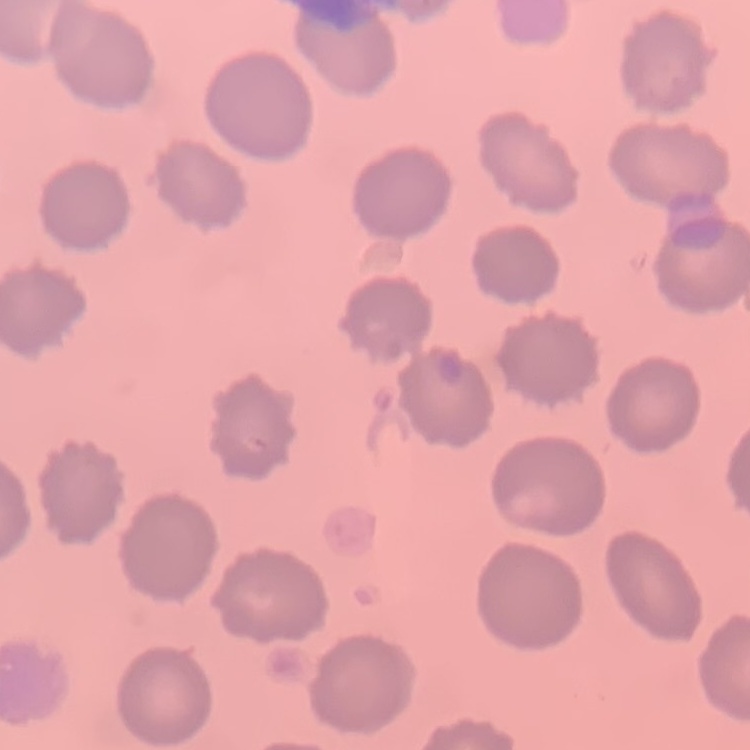
erythrocyte morphology = no rouleaux formation
preparation = thin blood smear
stain = Field's or Giemsa
image type = one tile cut from a larger photomicrograph